Assess this cell for malaria.
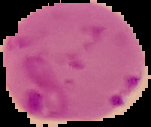
Parasitized.

Summary:
  - Image type: segmented cell region on a black background
  - Image size: 151×127 pixels
  - Preparation: thin blood film